Locate and identify every blood parasite.
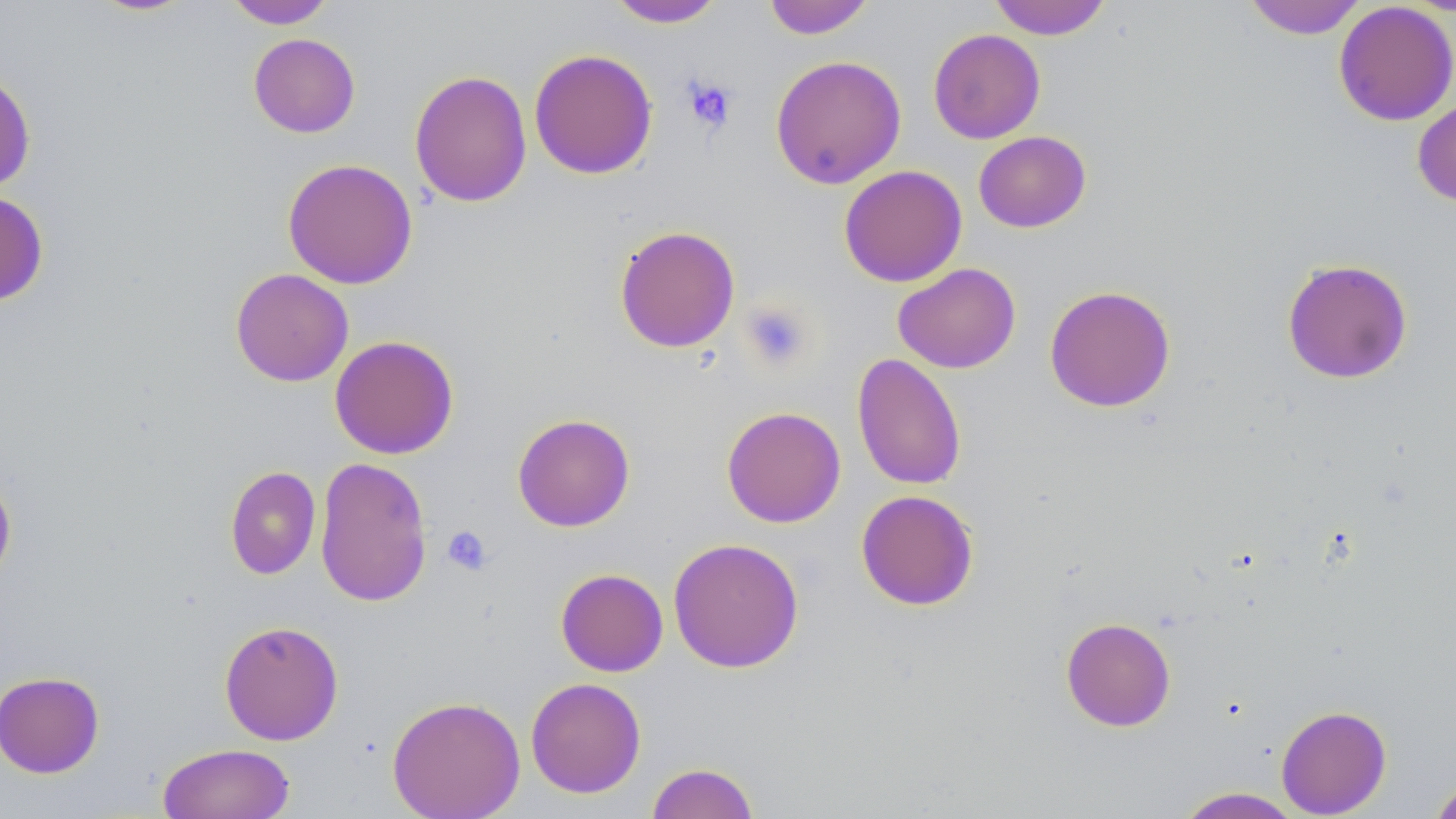

No blood parasites observed.

Approximate bounding boxes as (x1,y1)-(x2,y2) corner pairs in pixels. Uninfected red blood cell locations: (88,0)-(197,17), (224,0)-(336,29), (763,0)-(874,39), (988,0)-(1112,40), (1243,0)-(1367,39), (607,1)-(726,28), (1333,2)-(1456,126), (928,28)-(1045,144), (248,33)-(360,138), (529,48)-(658,180), (770,55)-(907,189), (0,66)-(36,194), (409,69)-(532,208), (1412,99)-(1456,207), (973,130)-(1091,233), (282,158)-(418,289), (838,165)-(967,287), (0,190)-(50,306), (614,225)-(740,353), (1281,258)-(1414,385), (892,262)-(1021,373), (230,268)-(354,387), (1044,284)-(1176,413), (330,335)-(459,459), (852,353)-(967,491), (721,406)-(846,528), (512,413)-(635,532), (314,455)-(433,608), (224,466)-(321,579), (0,472)-(17,587), (856,489)-(979,611), (667,537)-(804,673), (555,568)-(669,676), (1060,617)-(1176,732), (219,620)-(344,745), (0,671)-(105,778), (525,677)-(646,798), (387,695)-(525,819), (1276,704)-(1392,817), (156,743)-(295,819), (645,762)-(760,819), (1428,776)-(1456,819), (1173,787)-(1305,818). Platelet locations: (682,76)-(738,133), (740,300)-(813,372), (442,525)-(492,576). Slide-level diagnosis: no evidence of blood parasites. May-Grünwald-Giemsa stain. Thin blood film. Image is 1456×819 pixels. 1000x magnification. Light microscopy. One field of a larger specimen.